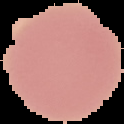
image size = 124×124 pixels
malaria status = uninfected
image type = segmented cell region on a black background
preparation = thin blood smear